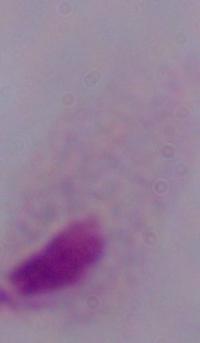
Summary:
  - Identification: trichomonad
  - Modality: micrograph
  - Magnification: 1000x